Assess the morphology of the red blood cells.
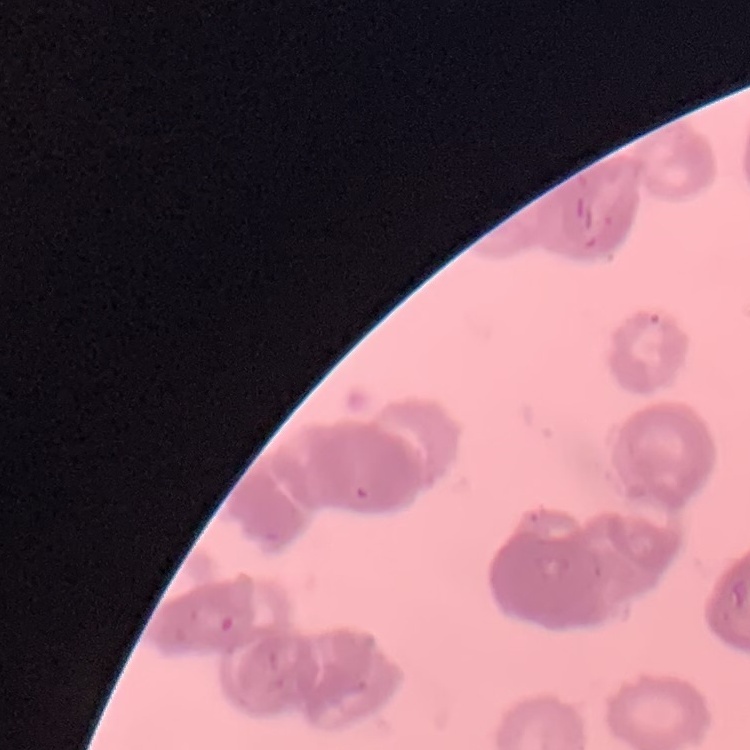

Rouleaux formation.

One tile cut from a larger photomicrograph. Stained with either Field's or Giemsa. Thin blood film.